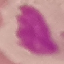
Summary:
  - Result: negative for malaria parasites
  - Image type: automatically extracted cell patch, resized to 64 × 64 pixels
  - Stain: Giemsa
  - Preparation: thin blood film
  - Capture: smartphone camera at the microscope eyepiece